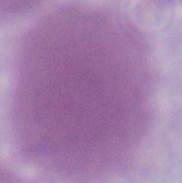 A red blood cell is seen. Photomicrograph. 1000x magnification.